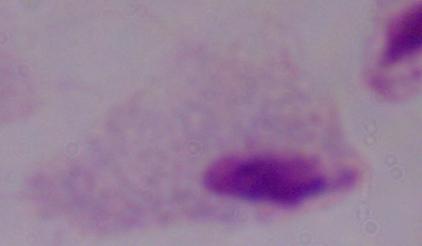

A trichomonad is shown. Micrograph. Captured at 1000x magnification.